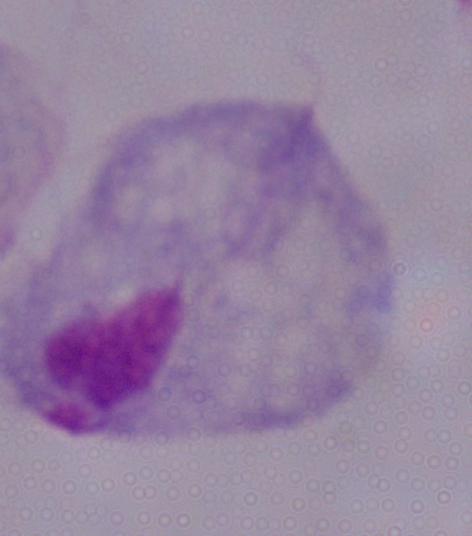
{
  "modality": "micrograph",
  "identification": "trichomonad",
  "magnification": "1000x"
}